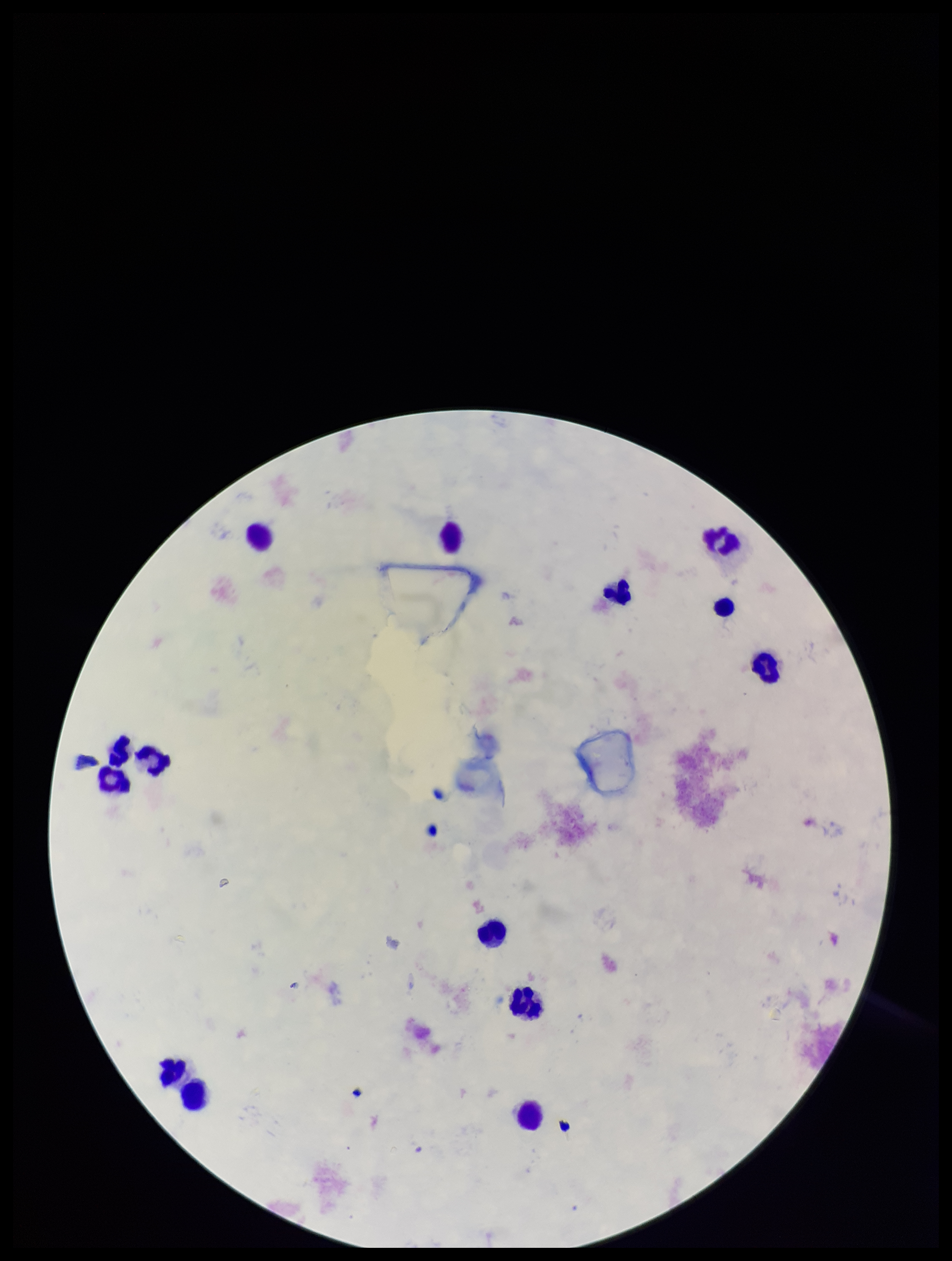

parasite_count: 0
stain: Giemsa
field_of_view: one from this slide
preparation: thick
patient_malaria_status: negative
plasmodium_parasites: none detected
image_size: 952×1261 pixels
leukocyte_count: 14
capture: smartphone photograph through the microscope eyepiece